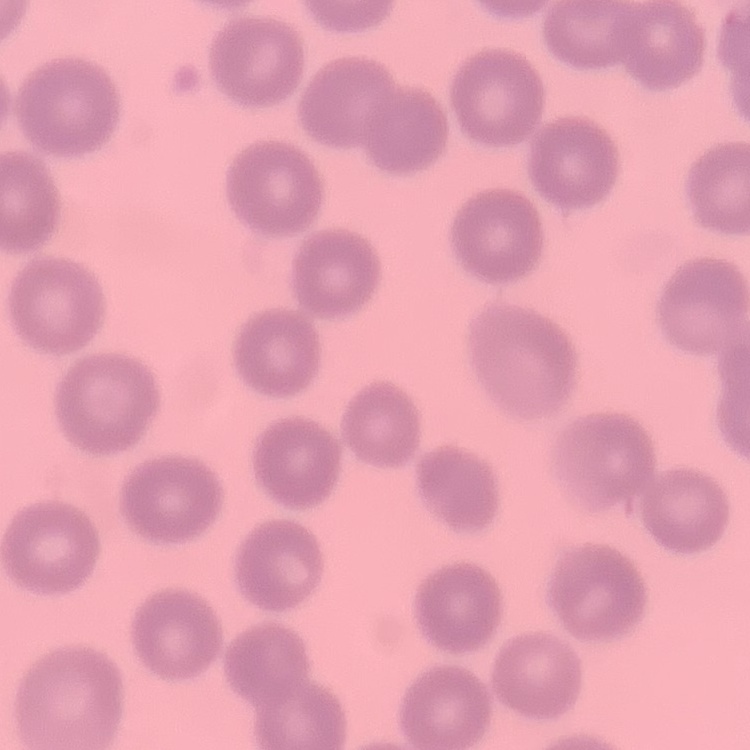
The red blood cells exhibit no rouleaux formation. One tile cut from a larger photomicrograph. Field's or Giemsa stain. Thin blood smear.